Classify this cell by malaria status.
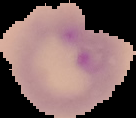

It is parasitized.

Summary:
  - Preparation: thin blood smear
  - Image type: cell region segmented out of the field of view; surrounding area masked to black
  - Image size: 136×118 pixels